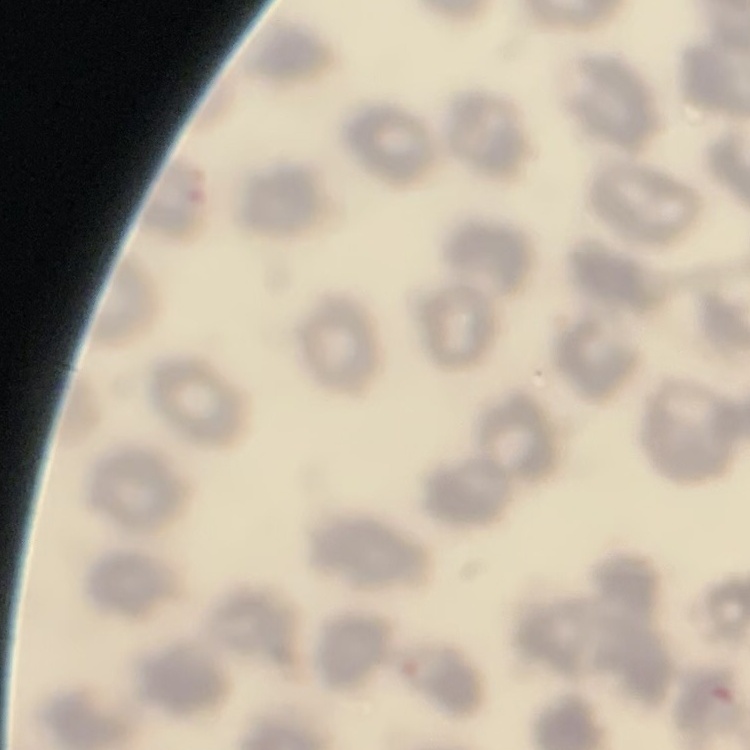

The erythrocytes exhibit no rouleaux formation. One tile cut from a larger photomicrograph. Field's or Giemsa stain. Thin blood smear.